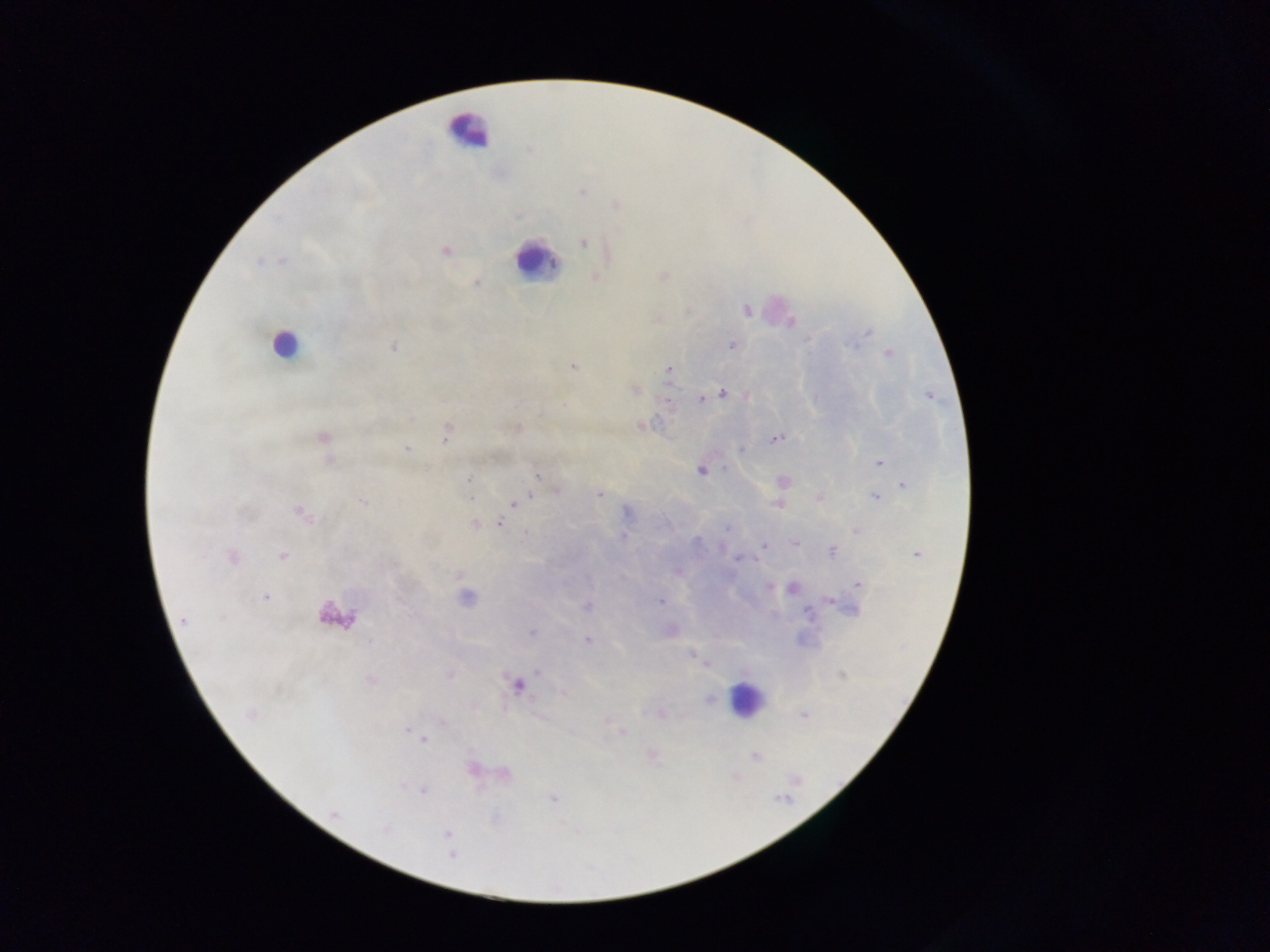
Approximate centers as {x, y} in pixels.
Summary:
  - Plasmodium parasite locations: {581, 190}, {615, 204}, {584, 242}, {445, 250}, {282, 260}, {662, 276}, {595, 277}, {476, 282}, {746, 310}, {790, 321}, {732, 345}, {393, 346}, {888, 353}, {573, 367}, {669, 369}, {634, 389}, {722, 392}, {929, 395}, {701, 399}, {669, 402}, {640, 424}, {515, 426}, {447, 431}, {323, 438}, {775, 438}, {406, 449}, {741, 449}, {879, 462}, {701, 469}, {537, 475}, {470, 478}, {782, 481}, {904, 484}, {557, 491}, {599, 494}, {529, 496}, {820, 496}, {877, 497}, {363, 501}, {514, 503}, {778, 503}, {511, 506}, {301, 513}, {500, 522}, {473, 523}, {856, 531}, {623, 536}, {793, 541}, {764, 544}, {831, 550}, {916, 553}, {282, 555}, {231, 557}, {677, 571}, {858, 583}, {792, 588}, {265, 597}, {465, 598}, {829, 599}, {660, 600}, {587, 606}, {851, 606}, {184, 621}, {669, 629}, {532, 632}, {587, 640}, {693, 654}, {370, 679}, {517, 684}, {563, 692}, {709, 699}, {250, 714}, {661, 714}, {804, 715}, {605, 719}, {622, 733}, {424, 740}, {651, 755}, {755, 755}, {471, 769}, {503, 772}, {423, 790}, {552, 799}, {334, 814}, {447, 834}, {451, 854}
  - Leukocyte locations: {468, 131}, {534, 261}, {282, 343}, {335, 615}, {745, 699}
  - Field of view: single
  - Image size: 1270×952 pixels
  - Capture: mobile-phone photograph through a microscope
  - Preparation: thick blood smear
  - Country: Ghana